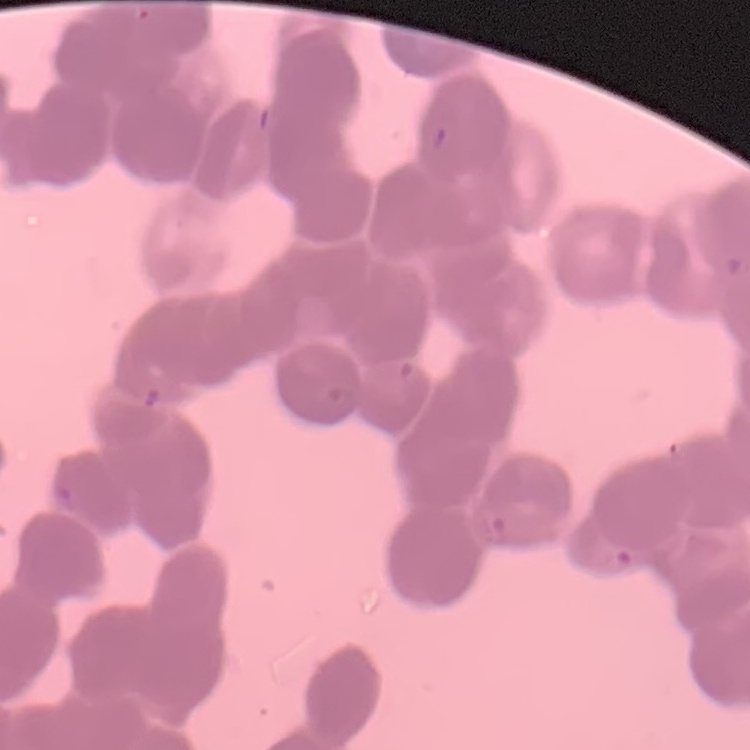
red_blood_cell_morphology: rouleaux formation
image_type: square crop of a larger photomicrograph
stain: Field's or Giemsa
preparation: thin blood smear